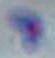
Photomicrograph. Toxoplasma gondii is seen. 1000x magnification.